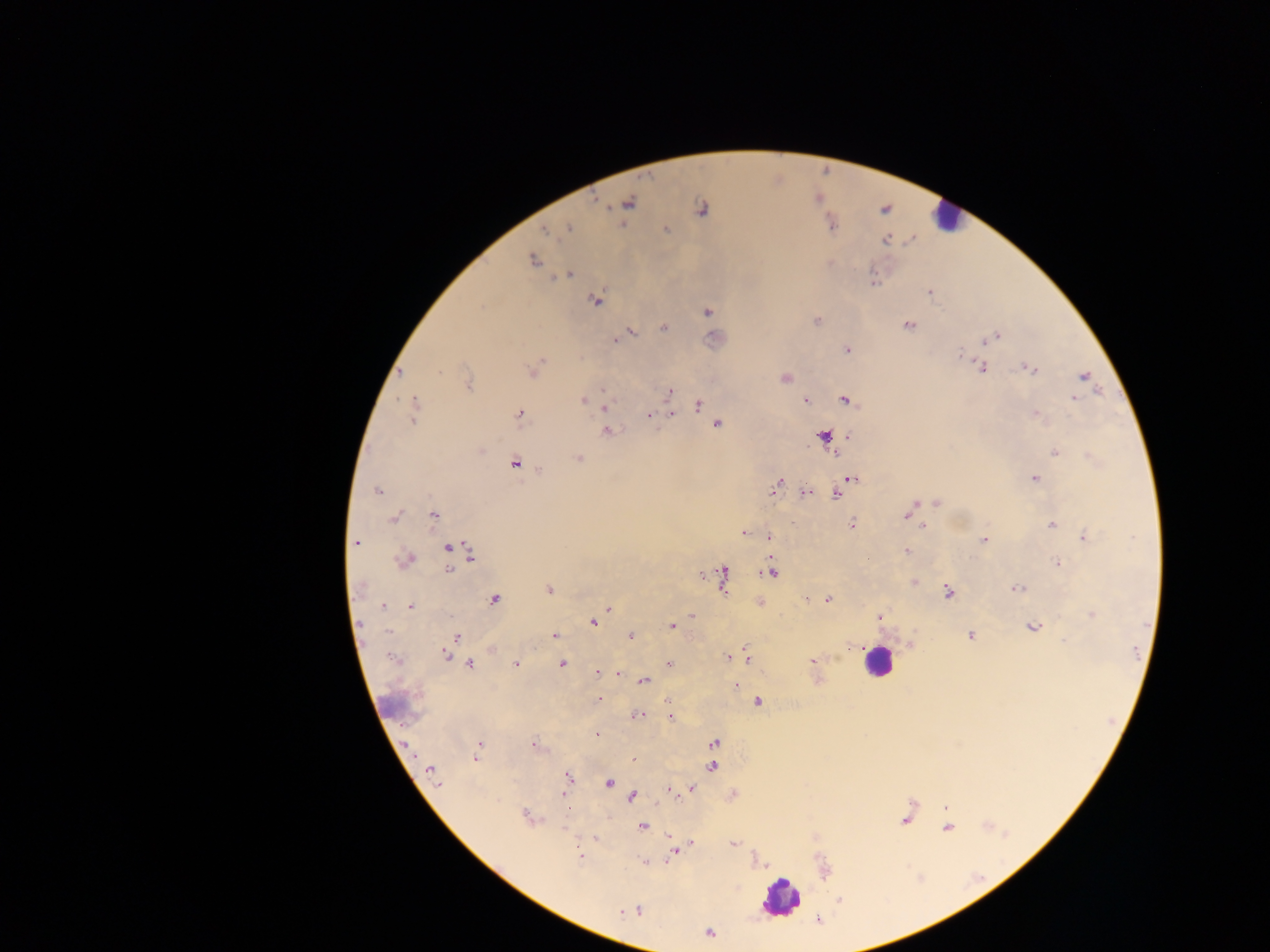

Approximate centers as x y in pixels. Leukocyte locations: 944 216; 876 662; 399 707; 781 898. Malaria parasite locations: 629 203; 701 210; 569 228; 666 230; 546 232; 885 240; 532 260; 567 275; 873 283; 930 292; 595 300; 481 307; 707 311; 816 320; 908 325; 664 327; 631 333; 995 337; 615 340; 985 341; 847 350; 961 353; 982 368; 532 369; 1030 369; 400 373; 1084 376; 785 379; 467 384; 603 389; 669 391; 1074 398; 582 400; 805 400; 846 401; 697 406; 604 407; 519 413; 413 414; 671 414; 1036 414; 648 416; 718 424; 607 431; 824 435; 480 450; 1055 452; 835 454; 579 459; 515 464; 539 470; 853 478; 1035 478; 777 486; 378 491; 806 492; 837 494; 937 502; 910 509; 907 514; 434 515; 394 517; 852 524; 1051 524; 922 526; 744 533; 769 536; 1084 537; 984 540; 357 542; 447 548; 907 550; 471 555; 406 559; 1057 563; 449 570; 771 572; 702 574; 724 574; 914 582; 358 588; 1016 588; 549 590; 948 592; 494 599; 807 599; 828 599; 383 606; 411 606; 608 608; 691 615; 1092 615; 880 617; 593 622; 672 626; 1033 627; 388 632; 554 635; 970 635; 630 636; 462 637; 1064 640; 446 654; 747 656; 727 657; 391 658; 813 660; 561 664; 669 664; 470 665; 516 665; 597 672; 620 675; 644 680; 736 686; 599 700; 669 701; 758 702; 637 716; 671 717; 598 735; 714 742; 534 745; 478 746; 476 758; 634 759; 712 767; 430 771; 568 777; 609 783; 690 789; 672 791; 564 793; 632 797; 946 807; 527 816; 904 820; 641 826; 948 828; 734 843; 692 844; 687 846; 673 853; 580 855; 644 862; 637 910; 621 912; 710 934. Single field of view. Image is 1270×952 pixels. Mobile-phone photograph taken through the microscope. Collected in Ghana. Thick blood smear.